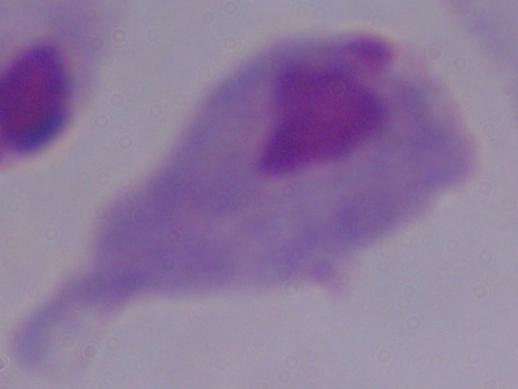

Photomicrograph. A trichomonad is shown. Captured at 1000x magnification.